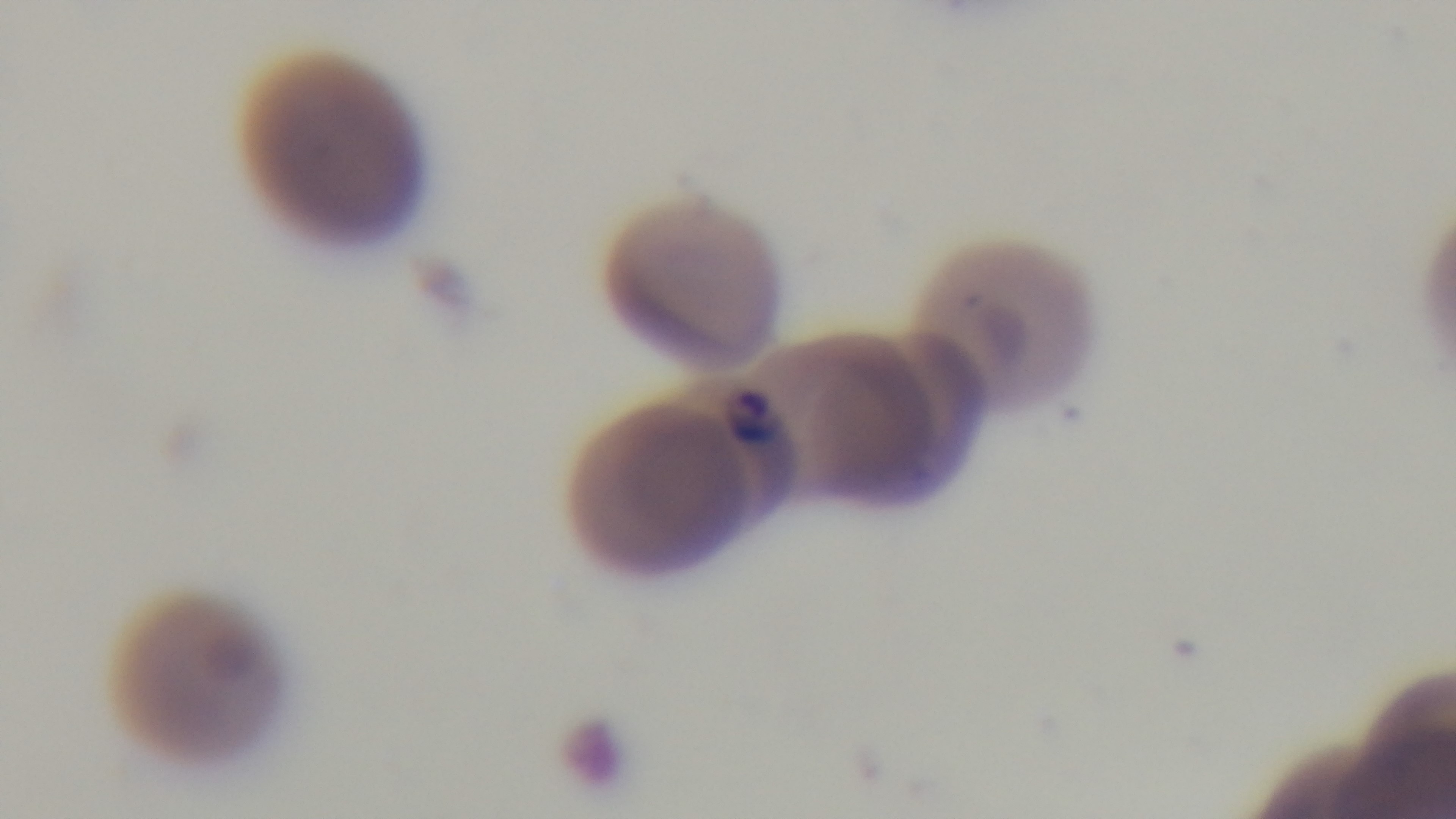
malaria status = positive
objective = 100x oil immersion
field of view = one from the slide
preparation = thin
stain = Giemsa
modality = light microscopy
capture = mounted 4K digital camera